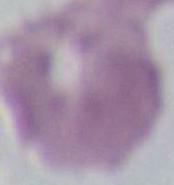
1000x magnification. An erythrocyte is seen. Photomicrograph.